Locate every blood parasite and identify its species.
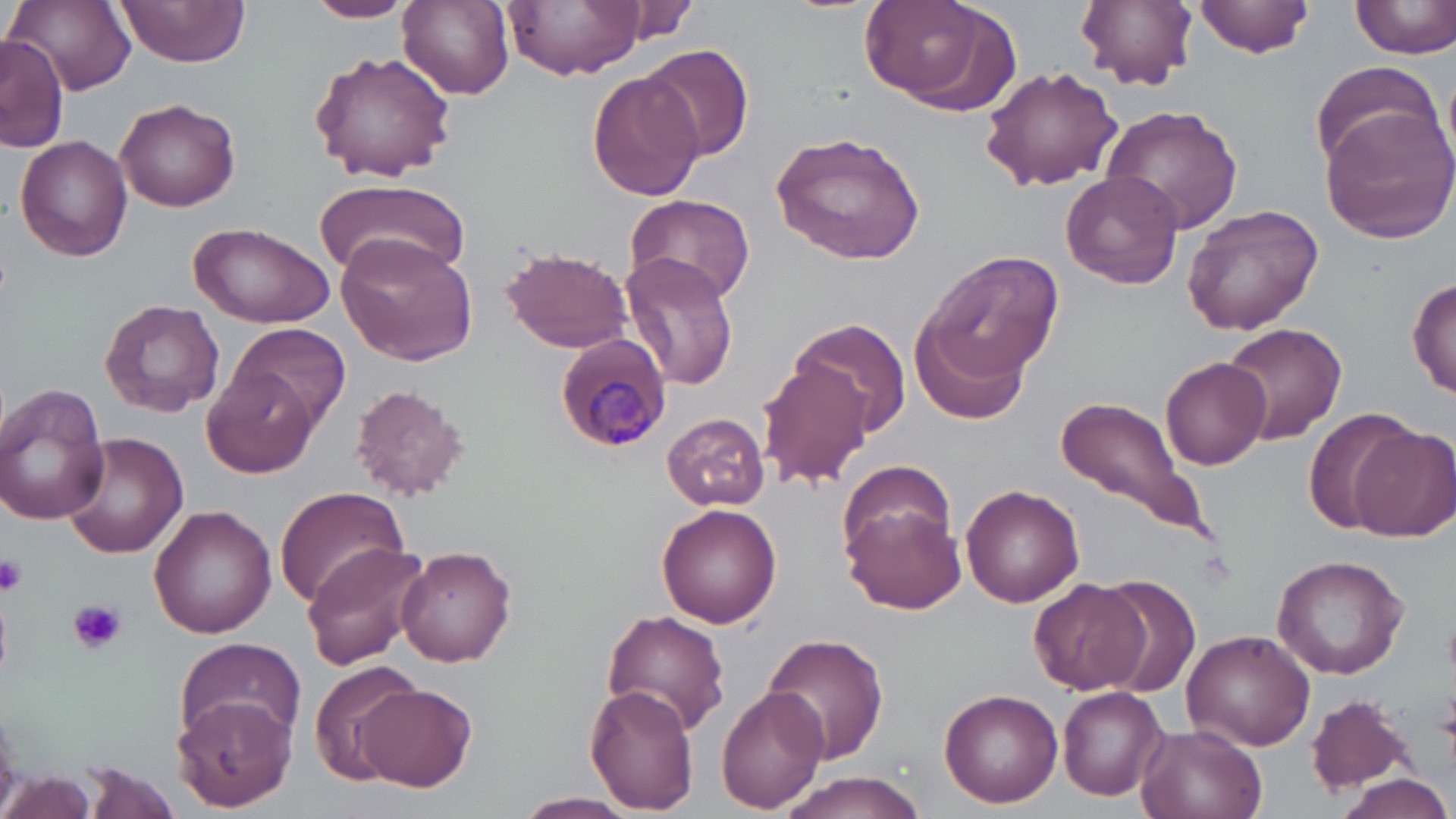

Approximate bounding boxes as (x1,y1)-(x2,y2) corner pairs in pixels.
Plasmodium malariae-infected red blood cells: (552,331)-(672,454).
No Plasmodium falciparum, Plasmodium ovale, Plasmodium vivax, Babesia divergens, or Trypanosoma brucei observed.

Uninfected red blood cell locations: (113,0)-(250,68), (306,0)-(412,23), (397,0)-(515,99), (506,0)-(642,79), (857,0)-(1007,108), (1077,0)-(1196,90), (1193,0)-(1314,57), (1350,0)-(1456,60), (613,1)-(700,44), (11,3)-(135,92), (1,36)-(68,153), (639,43)-(754,162), (308,52)-(457,181), (1309,60)-(1437,169), (980,65)-(1122,191), (588,71)-(706,201), (113,97)-(241,211), (1100,104)-(1243,238), (1323,108)-(1456,242), (769,130)-(926,265), (15,136)-(134,263), (1060,171)-(1182,290), (315,180)-(471,282), (625,192)-(756,307), (1183,204)-(1324,334), (189,220)-(333,327), (335,232)-(480,367), (499,248)-(633,353), (923,252)-(1066,380), (621,254)-(740,390), (1407,274)-(1456,402), (100,299)-(225,418), (792,318)-(912,438), (913,318)-(1029,426), (1219,321)-(1347,445), (228,323)-(354,430), (1161,356)-(1272,470), (754,359)-(875,489), (202,367)-(318,477), (348,383)-(469,500), (0,385)-(111,525), (1054,393)-(1211,539), (1302,407)-(1418,536), (663,414)-(769,510), (1353,423)-(1456,541), (59,430)-(188,559), (838,457)-(957,566), (272,485)-(408,610), (962,485)-(1084,608), (845,501)-(969,614), (656,502)-(781,625), (149,504)-(276,638), (300,542)-(429,670), (397,546)-(517,667), (1272,555)-(1410,679), (1091,579)-(1203,700), (1027,580)-(1149,695), (599,610)-(731,737), (1182,629)-(1315,751), (763,632)-(890,767), (175,636)-(306,748), (308,658)-(427,785), (356,682)-(477,792), (585,684)-(700,812), (715,685)-(828,813), (1057,685)-(1170,800), (939,689)-(1062,807), (172,694)-(298,812), (1304,694)-(1414,793), (1138,727)-(1263,819), (78,762)-(186,819), (1,771)-(98,818), (771,771)-(934,819), (1338,773)-(1452,819), (513,791)-(642,818). Platelet locations: (0,552)-(29,598), (69,598)-(127,654). Slide-level diagnosis: Plasmodium malariae. May-Grünwald-Giemsa stain. Thin blood film. Light microscopy. Captured at 1000x magnification. Image is 1456×819 pixels. One field of a larger specimen.